Point out each Plasmodium parasite.
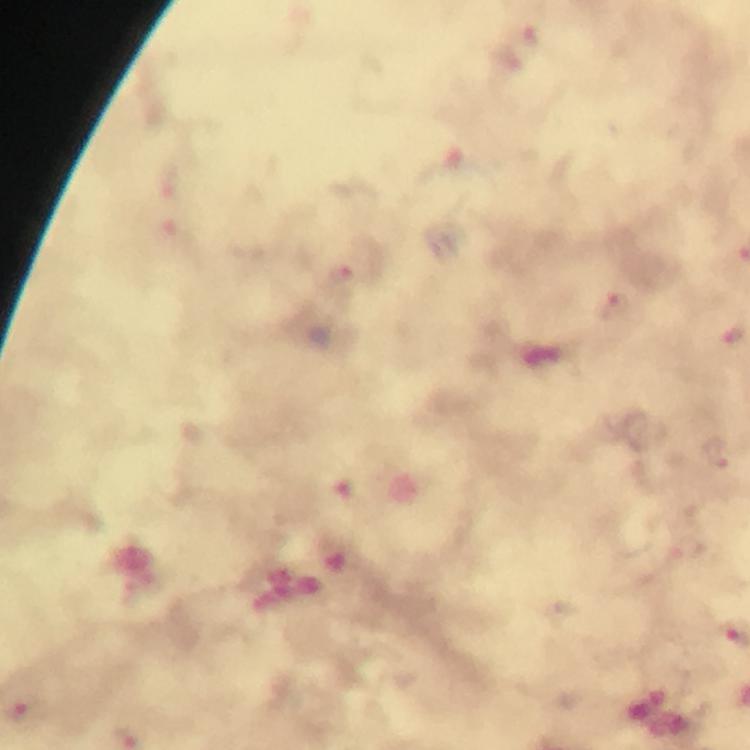
Approximate centers as {x, y} in pixels.
Plasmodium parasites: {614, 304}, {716, 454}, {21, 714}.

Summary:
  - Preparation: thick blood film
  - Stain: Giemsa
  - Immersion oil: applied
  - Magnification: 100x
  - Cropped from: a single field of view
  - Context: from a malaria diagnostic workup
  - Image size: 750×750 pixels
  - Capture: smartphone photograph through a microscope